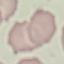
Result: no malaria parasites detected. Cell patch, automatically extracted from a larger field of view and resized to 64 × 64 pixels. Photographed with a smartphone camera at the microscope eyepiece. Giemsa stain. Thin blood film.